Assess this cell for malaria.
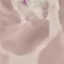
Uninfected.

preparation: thin smear
image_type: cell patch, automatically extracted from a larger field of view and resized to 64 × 64 pixels
stain: Giemsa
capture: smartphone camera at the microscope eyepiece